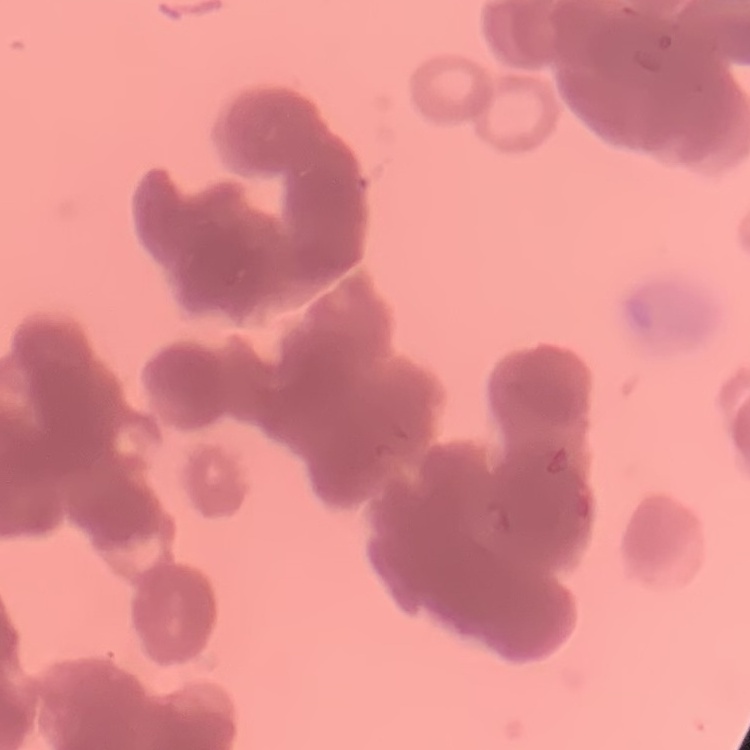
Summary:
  - Erythrocyte morphology: rouleaux formation
  - Preparation: thin blood film
  - Image type: square crop of a larger photomicrograph
  - Stain: Field's or Giemsa